Identify the preparation type.
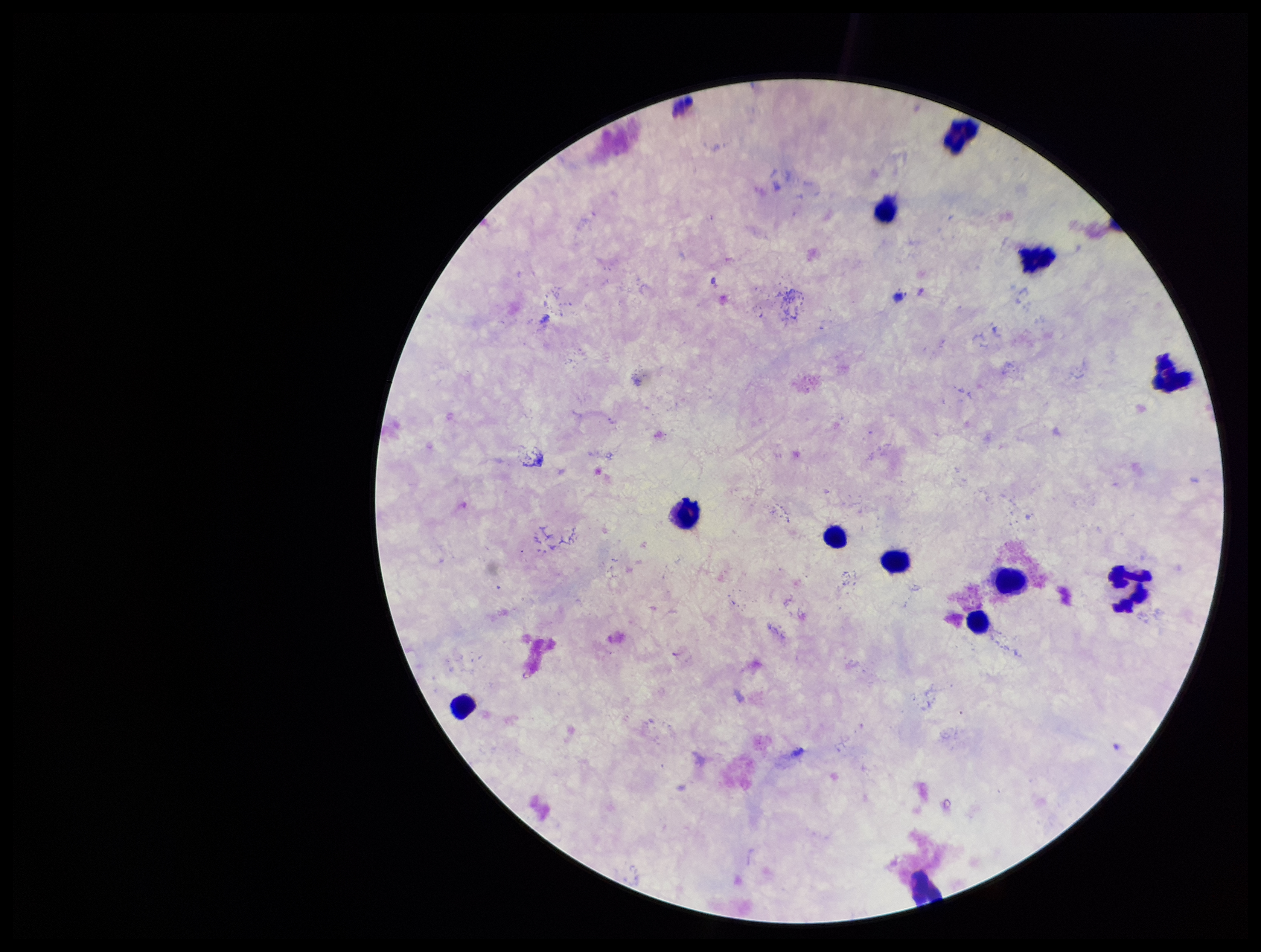

It is a thick blood smear.

Patient malaria status: negative. Image is 1261×952 pixels. Parasite count: 0. One field from this slide. Photographed through the microscope eyepiece with a smartphone camera. Leukocyte count: 11. Stained with Giemsa. Plasmodium parasites: none seen.